Classify this cell by malaria status.
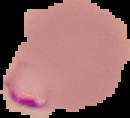

Parasitized.

image type = segmented cell region with the area outside set to black
image size = 130×118 pixels
preparation = thin blood smear